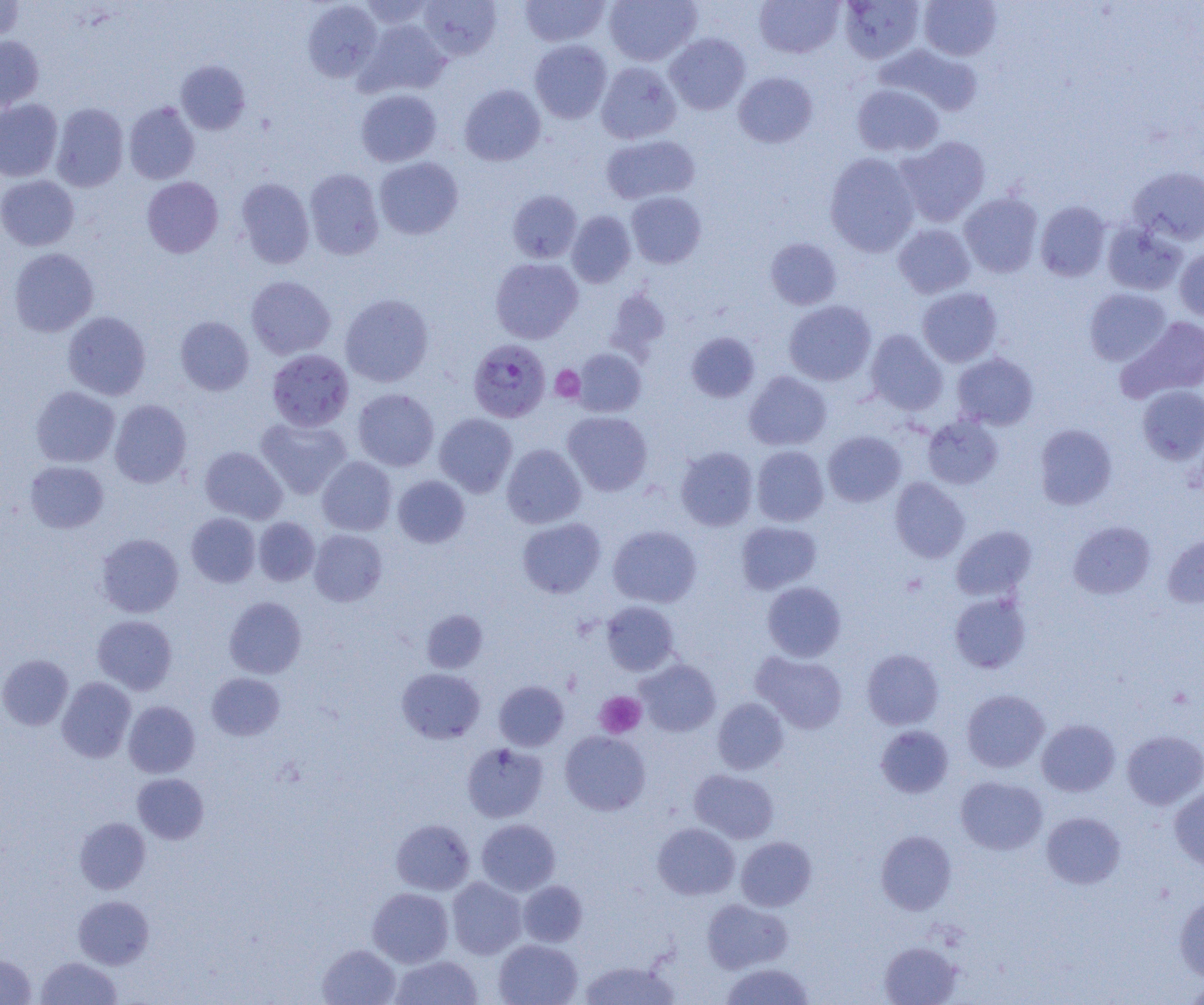

slide-level diagnosis = Plasmodium falciparum
image size = 1204×1005 pixels
magnification = 1000x
field of view = single
platelet locations = approximate bounding boxes as (x1,y1)-(x2,y2) corner pairs in pixels: (551,366)-(585,402), (901,573)-(928,597), (595,691)-(646,738)
Plasmodium falciparum-infected red blood cell locations = approximate bounding boxes as (x1,y1)-(x2,y2) corner pairs in pixels: (468,339)-(551,422)
uninfected red blood cell locations = approximate bounding boxes as (x1,y1)-(x2,y2) corner pairs in pixels: (357,0)-(436,29), (520,0)-(609,47), (604,0)-(702,66), (754,0)-(845,59), (839,0)-(925,63), (919,0)-(1002,61), (0,1)-(25,43), (302,1)-(382,82), (418,1)-(501,60), (359,20)-(450,97), (665,33)-(751,114), (0,35)-(44,112), (529,39)-(612,123), (877,44)-(982,117), (175,60)-(251,135), (596,62)-(682,144), (734,72)-(818,148), (851,83)-(944,157), (459,84)-(545,166), (355,89)-(442,167), (0,99)-(62,181), (124,102)-(200,184), (51,103)-(129,191), (601,134)-(700,204), (895,135)-(991,227), (825,152)-(920,256), (374,157)-(463,240), (1128,166)-(1204,245), (304,168)-(384,260), (0,175)-(79,251), (142,176)-(223,257), (235,178)-(315,268), (507,190)-(582,263), (626,192)-(706,268), (959,192)-(1043,278), (1036,201)-(1111,281), (566,210)-(636,287), (1102,222)-(1187,296), (893,223)-(975,298), (765,238)-(842,309), (9,248)-(99,337), (1175,248)-(1204,321), (490,258)-(583,343), (246,275)-(336,360), (604,287)-(671,361), (917,287)-(1002,367), (1084,288)-(1171,366), (340,293)-(433,387), (784,300)-(876,385), (63,311)-(151,400), (175,316)-(254,396), (1116,316)-(1204,403), (864,330)-(948,415), (685,331)-(760,402), (573,348)-(647,417), (267,349)-(354,431), (952,352)-(1039,430), (744,371)-(832,451), (1137,385)-(1204,465), (30,386)-(120,467), (353,388)-(439,471), (109,400)-(191,488), (562,411)-(652,496), (434,413)-(517,497), (256,416)-(352,499), (923,416)-(1003,489), (1034,424)-(1117,509), (823,430)-(906,507), (502,444)-(586,528), (752,445)-(829,526), (200,446)-(287,524), (675,447)-(758,531), (317,456)-(397,536), (25,461)-(109,533), (393,475)-(470,548), (890,477)-(970,563), (186,513)-(260,587), (253,517)-(320,586), (517,517)-(605,598), (736,521)-(822,594), (1068,521)-(1155,599), (608,525)-(701,607), (951,526)-(1036,601), (309,529)-(387,606), (96,533)-(184,618), (1162,533)-(1204,608), (762,581)-(846,661), (950,593)-(1030,673), (224,596)-(306,678), (601,601)-(679,675), (421,609)-(488,673), (92,615)-(177,694), (862,648)-(944,729), (752,652)-(848,733), (0,654)-(73,731), (636,659)-(720,736), (397,667)-(485,743), (207,672)-(284,740), (57,677)-(136,762), (494,680)-(569,751), (962,689)-(1049,773), (712,697)-(788,774), (123,701)-(200,777), (1037,719)-(1120,796), (875,725)-(954,798), (560,730)-(650,815), (1122,730)-(1204,809), (462,743)-(548,822), (690,769)-(779,843), (132,773)-(209,844), (956,776)-(1048,855), (1169,785)-(1204,871), (1041,812)-(1125,889), (75,818)-(150,894), (391,818)-(474,895), (476,819)-(560,896), (653,823)-(740,900), (876,830)-(957,914), (736,836)-(816,911), (447,877)-(527,959), (518,880)-(587,947), (368,888)-(453,967), (73,895)-(153,969), (1174,895)-(1204,982), (702,898)-(792,973), (493,939)-(582,1005), (879,941)-(962,1005), (318,944)-(400,1005), (0,954)-(36,1005), (389,955)-(483,1005), (36,956)-(122,1004), (579,959)-(679,1004), (720,963)-(814,1005), (1182,981)-(1204,1003)
modality = optical microscopy
preparation = thin blood smear